Locate every blood parasite and identify its species.
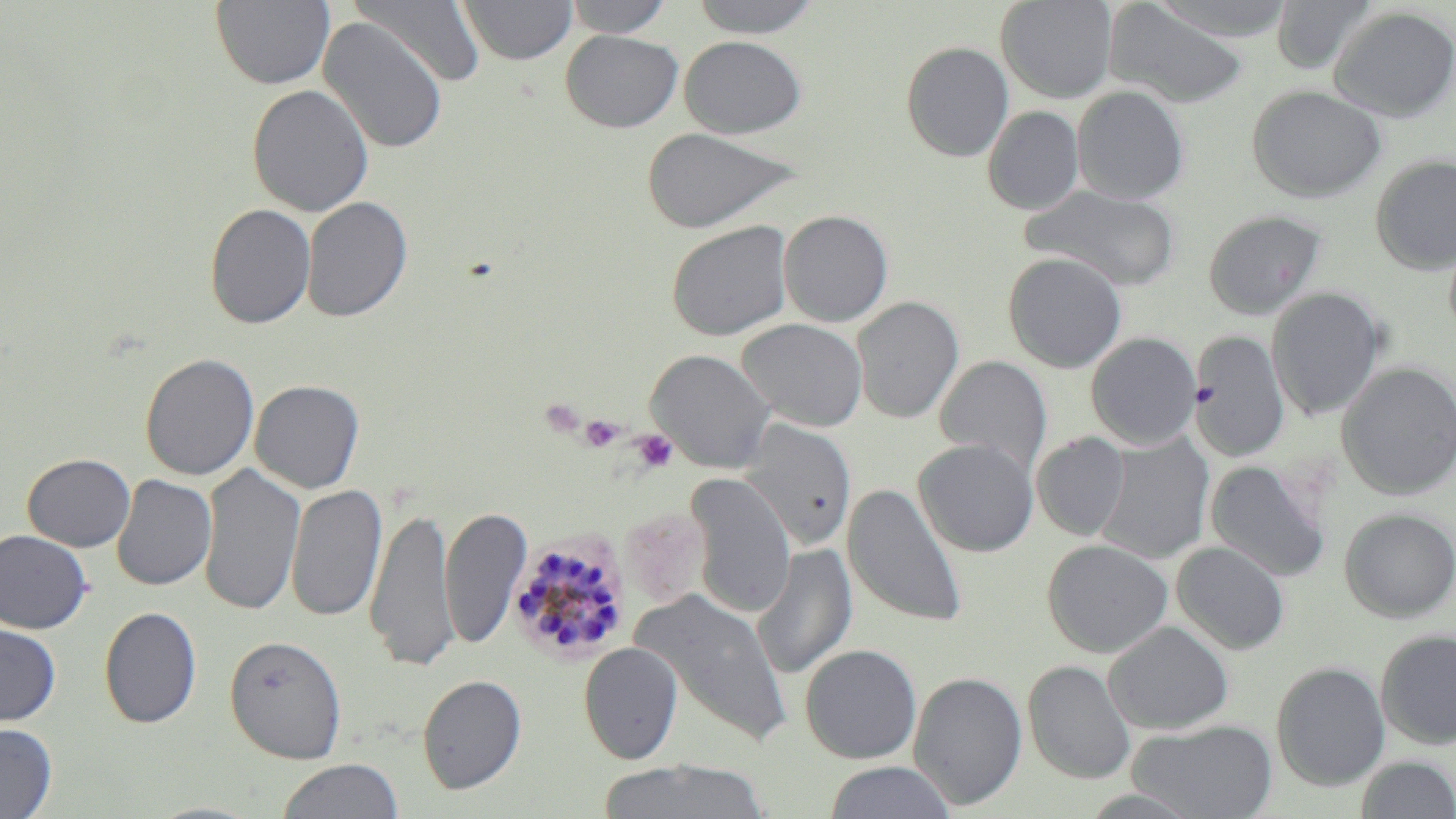
Approximate bounding boxes as (x1, y1, x2, y2) in pixels.
Plasmodium malariae-infected red blood cells: (508, 527, 631, 664).
No Plasmodium falciparum, Plasmodium ovale, Plasmodium vivax, Babesia divergens, or Trypanosoma brucei observed.

Summary:
  - Platelet locations: (579, 415, 625, 451), (632, 429, 678, 473)
  - Uninfected red blood cell locations: (210, 0, 336, 90), (459, 0, 577, 65), (563, 0, 674, 38), (688, 0, 824, 38), (996, 0, 1117, 104), (1147, 0, 1298, 42), (1270, 0, 1378, 75), (351, 1, 486, 89), (1105, 3, 1248, 108), (1328, 6, 1456, 122), (318, 16, 449, 155), (560, 29, 683, 133), (681, 36, 806, 138), (900, 41, 1014, 162), (247, 83, 374, 217), (1246, 84, 1387, 203), (1072, 85, 1189, 204), (982, 106, 1085, 215), (641, 127, 801, 233), (1370, 155, 1456, 274), (1020, 186, 1180, 290), (302, 196, 413, 323), (204, 203, 316, 329), (1203, 209, 1326, 320), (778, 210, 893, 327), (666, 221, 793, 341), (1003, 252, 1127, 373), (1267, 287, 1386, 421), (851, 296, 964, 424), (737, 318, 868, 432), (1190, 330, 1289, 462), (1086, 331, 1202, 449), (646, 349, 775, 473), (139, 352, 259, 481), (934, 355, 1053, 477), (1336, 362, 1456, 500), (249, 379, 364, 493), (739, 418, 857, 551), (1031, 432, 1131, 541), (1094, 433, 1215, 564), (914, 438, 1039, 557), (22, 453, 136, 551), (1205, 459, 1332, 583), (199, 462, 305, 617), (112, 474, 216, 591), (686, 475, 796, 619), (286, 483, 387, 623), (843, 483, 967, 629), (365, 504, 458, 672), (441, 506, 532, 650), (620, 507, 709, 609), (1339, 508, 1456, 622), (0, 530, 93, 634), (1042, 539, 1173, 658), (1172, 541, 1289, 654), (752, 543, 858, 680), (633, 591, 792, 746), (99, 606, 202, 728), (1104, 621, 1233, 735), (0, 622, 61, 726), (1376, 629, 1456, 749), (224, 634, 347, 763), (579, 642, 683, 764), (799, 643, 922, 764), (1023, 660, 1136, 784), (1271, 661, 1391, 791), (908, 670, 1028, 810), (417, 674, 527, 794), (1129, 718, 1278, 819), (1, 722, 57, 818), (1355, 755, 1456, 818), (275, 758, 405, 818), (594, 759, 771, 819), (822, 761, 958, 819), (144, 800, 269, 819)
  - Slide-level diagnosis: Plasmodium malariae
  - Image size: 1456×819 pixels
  - Modality: light microscopy
  - Preparation: thin blood film
  - Stain: May-Grünwald-Giemsa
  - Field of view: single
  - Magnification: 1000x